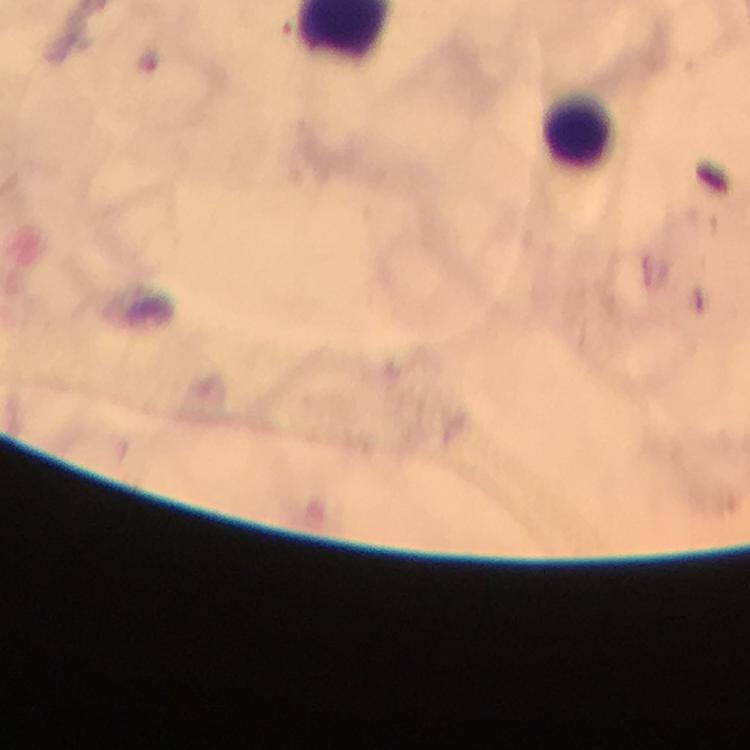

Approximate centers as {x, y} in pixels.
Summary:
  - Leukocyte locations: {581, 137}
  - Preparation: thick blood film
  - Stain: Giemsa
  - Malaria parasites: none detected
  - Image size: 750×750 pixels
  - Magnification: 100x
  - Immersion oil: applied
  - Context: from a malaria diagnostic workup
  - Cropped from: one field of view
  - Capture: smartphone photograph through a microscope